Name the parasite shown.
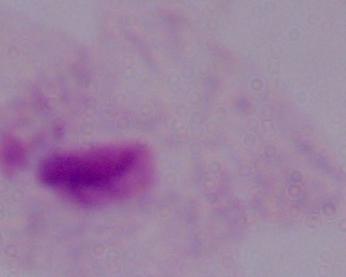

This is a trichomonad.

Summary:
  - Magnification: 1000x
  - Modality: micrograph